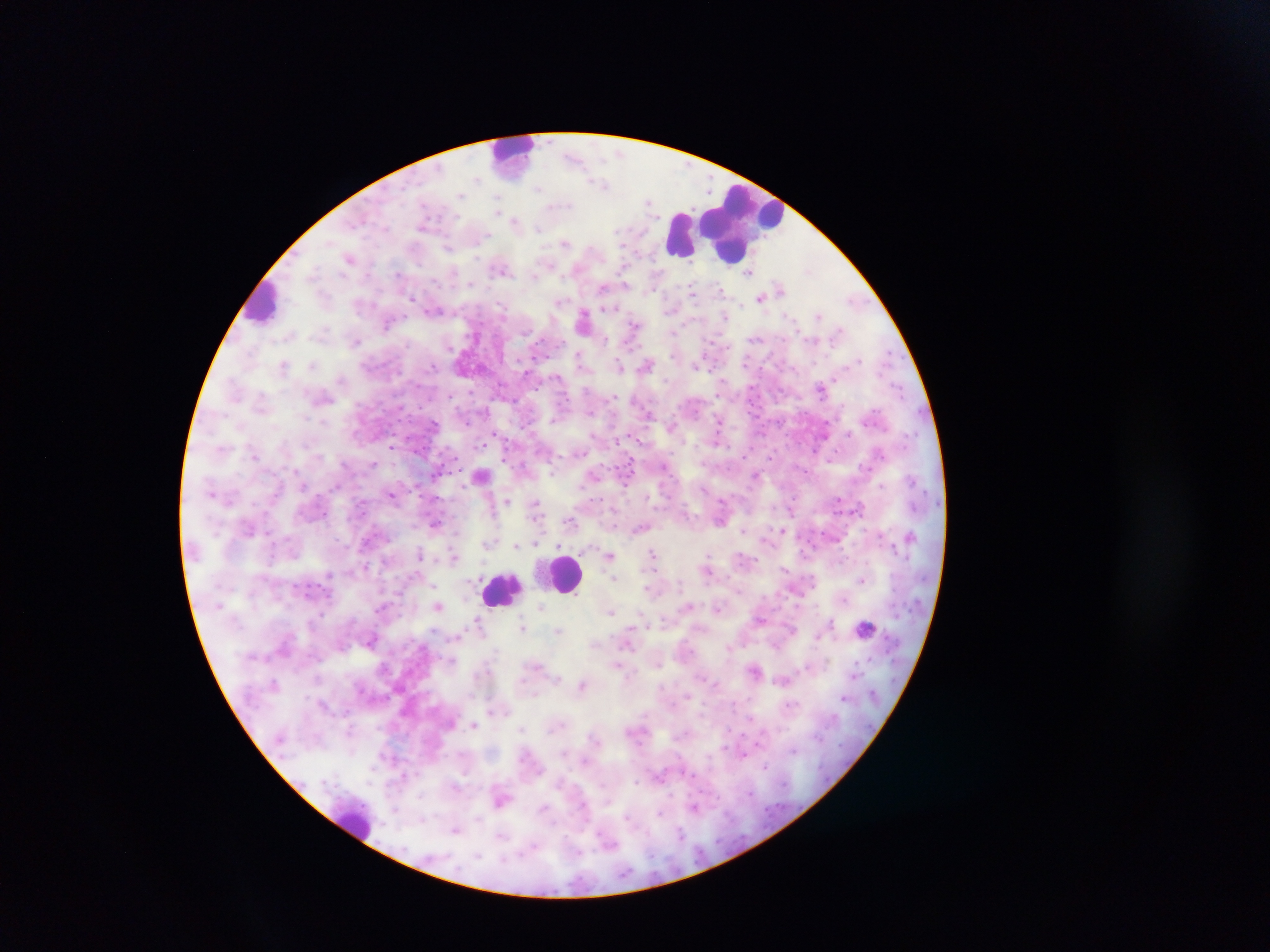
image size = 1270×952 pixels
malaria parasite locations = approximate centers as (x, y) in pixels: (603, 184), (648, 203), (516, 221), (565, 243), (449, 247), (351, 257), (502, 268), (750, 271), (604, 287), (780, 289), (693, 295), (761, 298), (853, 299), (434, 310), (725, 315), (820, 315), (584, 319), (388, 322), (634, 327), (357, 340), (580, 358), (284, 365), (619, 365), (697, 365), (313, 366), (647, 366), (822, 389), (718, 423), (672, 427), (496, 434), (391, 446), (255, 455), (481, 475), (594, 475), (756, 476), (338, 485), (417, 486), (392, 493), (838, 499), (507, 502), (535, 506), (791, 510), (613, 511), (571, 521), (435, 524), (641, 527), (782, 529), (743, 530), (267, 534), (910, 536), (488, 543), (535, 543), (517, 545), (653, 554), (421, 555), (609, 555), (454, 556), (785, 568), (708, 570), (614, 578), (862, 580), (650, 588), (439, 606), (542, 606), (688, 606), (717, 607), (611, 611), (760, 619), (478, 622), (829, 622), (523, 628), (864, 628), (559, 629), (371, 640), (618, 664), (536, 665), (756, 669), (853, 676), (783, 680), (275, 683), (583, 686), (845, 697), (474, 725), (766, 766), (501, 799), (695, 807), (457, 830), (500, 836)
leukocyte locations = approximate centers as (x, y) in pixels: (513, 154), (739, 223), (680, 236), (263, 301), (565, 574), (502, 591), (355, 821)
field of view = single
capture = mobile-phone photograph through a microscope
preparation = thick blood smear
country = Ghana